Comment on the morphology of the erythrocytes.
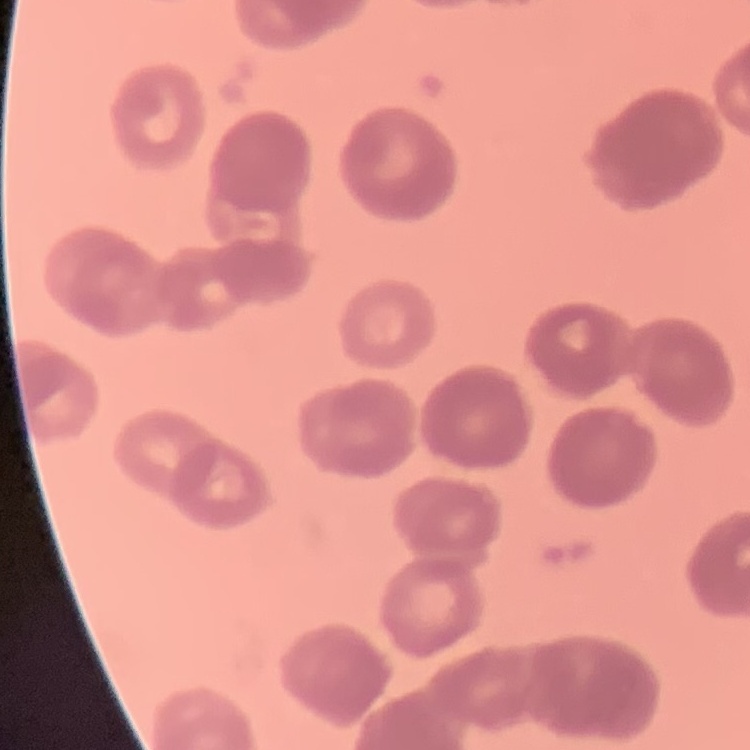
They show rouleaux formation.

preparation = thin peripheral smear
stain = Field's or Giemsa
image type = one tile cut from a larger photomicrograph